Point out each Plasmodium parasite.
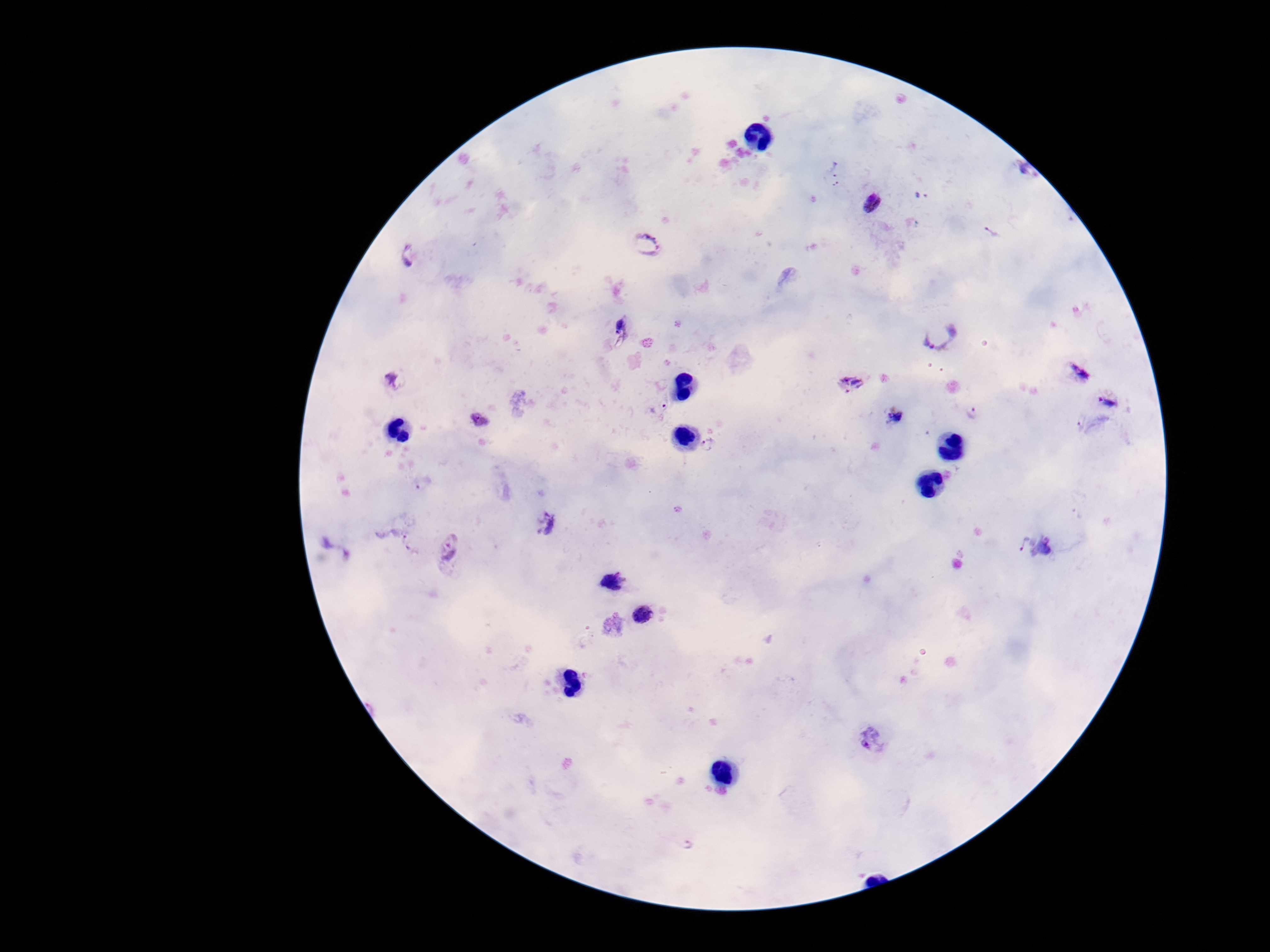
Approximate object centers, in pixels from the top-left corner.
Plasmodium parasites: (x=834, y=174), (x=1022, y=174), (x=922, y=195), (x=871, y=204), (x=992, y=232), (x=645, y=244), (x=411, y=257), (x=621, y=329), (x=941, y=339), (x=1079, y=373), (x=397, y=379), (x=852, y=383), (x=1110, y=403), (x=659, y=409), (x=972, y=413), (x=895, y=417), (x=479, y=420), (x=710, y=445), (x=424, y=483), (x=548, y=525), (x=410, y=543), (x=1037, y=544), (x=449, y=547), (x=614, y=582), (x=643, y=615), (x=874, y=740), (x=689, y=845).

field of view = single
patient malaria status = infected
magnification = 100x
preparation = thick blood smear
stain = Giemsa
image size = 1270×952 pixels
capture = smartphone camera through the microscope eyepiece